Name the parasite shown.
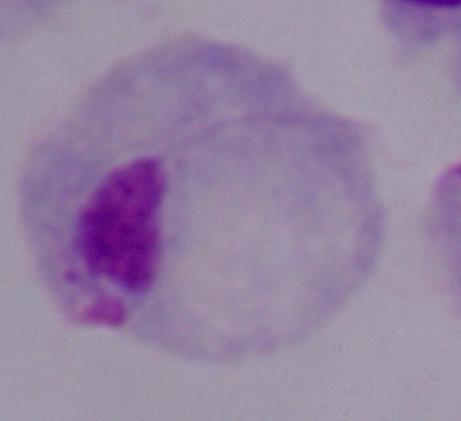
A trichomonad.

1000x magnification. Photomicrograph.